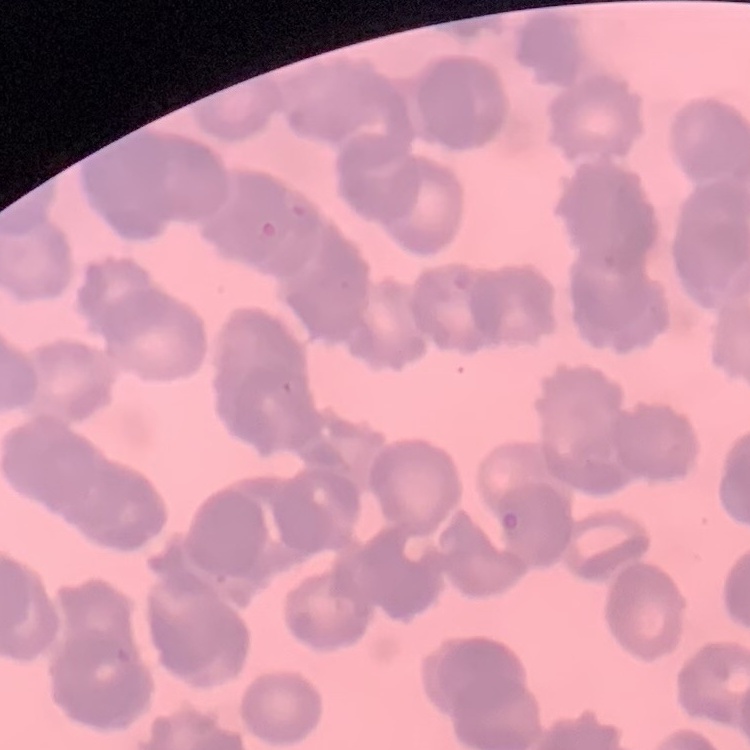 The red blood cells show rouleaux formation. One tile cut from a larger photomicrograph. Stained with either Field's or Giemsa. Thin blood smear.